Report the malaria status of this cell.
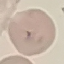

It is uninfected.

Summary:
  - Image type: cell patch, automatically extracted from a larger field of view and resized to 64 × 64 pixels
  - Preparation: thin smear
  - Stain: Giemsa
  - Capture: smartphone camera at the microscope eyepiece